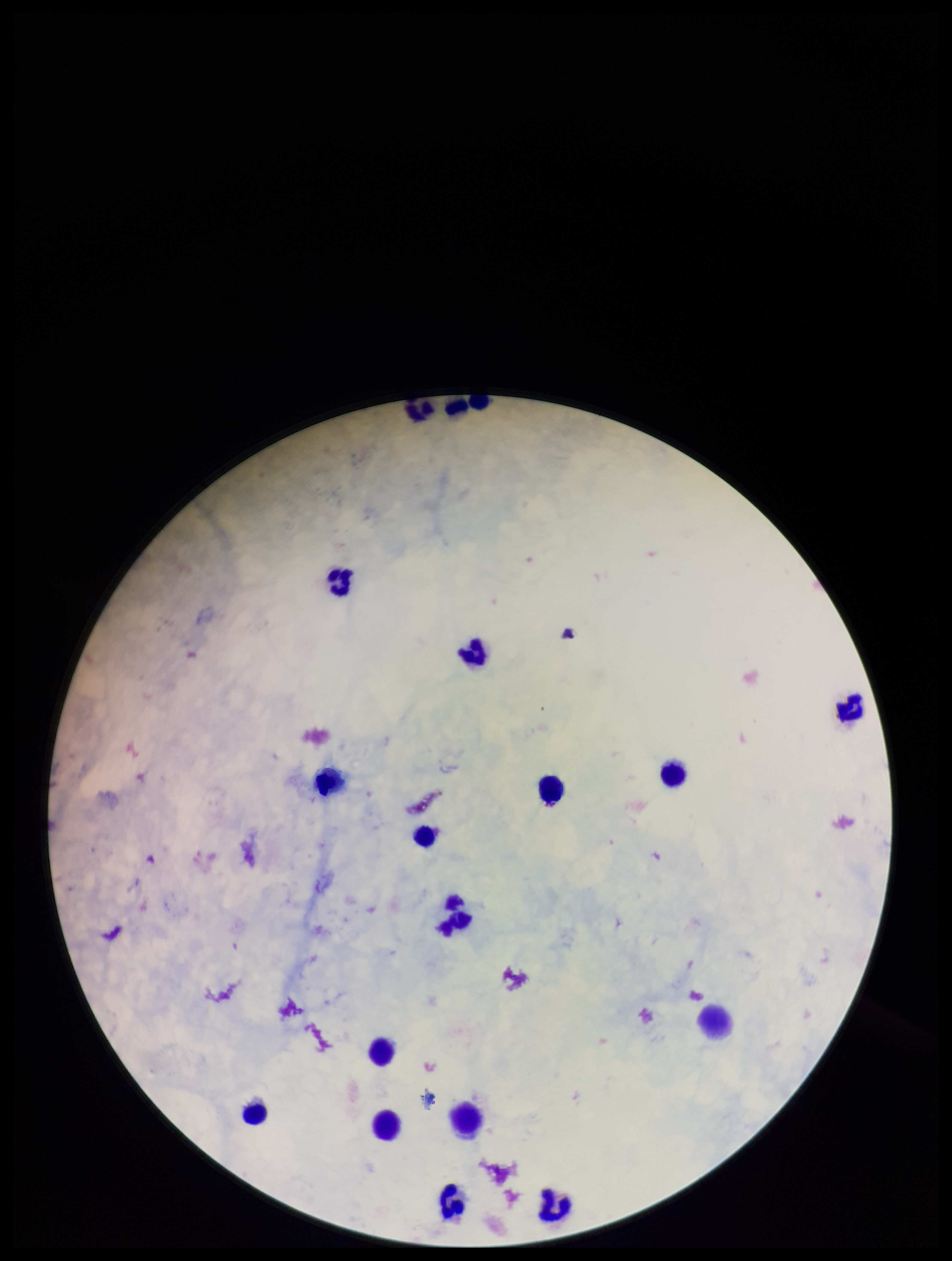

Summary:
  - Parasite count: 0
  - Plasmodium parasites: none identified
  - Image size: 952×1261 pixels
  - Capture: smartphone photograph through the microscope eyepiece
  - Field of view: one from this slide
  - Preparation: thick blood smear
  - Patient malaria status: negative
  - Stain: Giemsa
  - Leukocyte count: 18